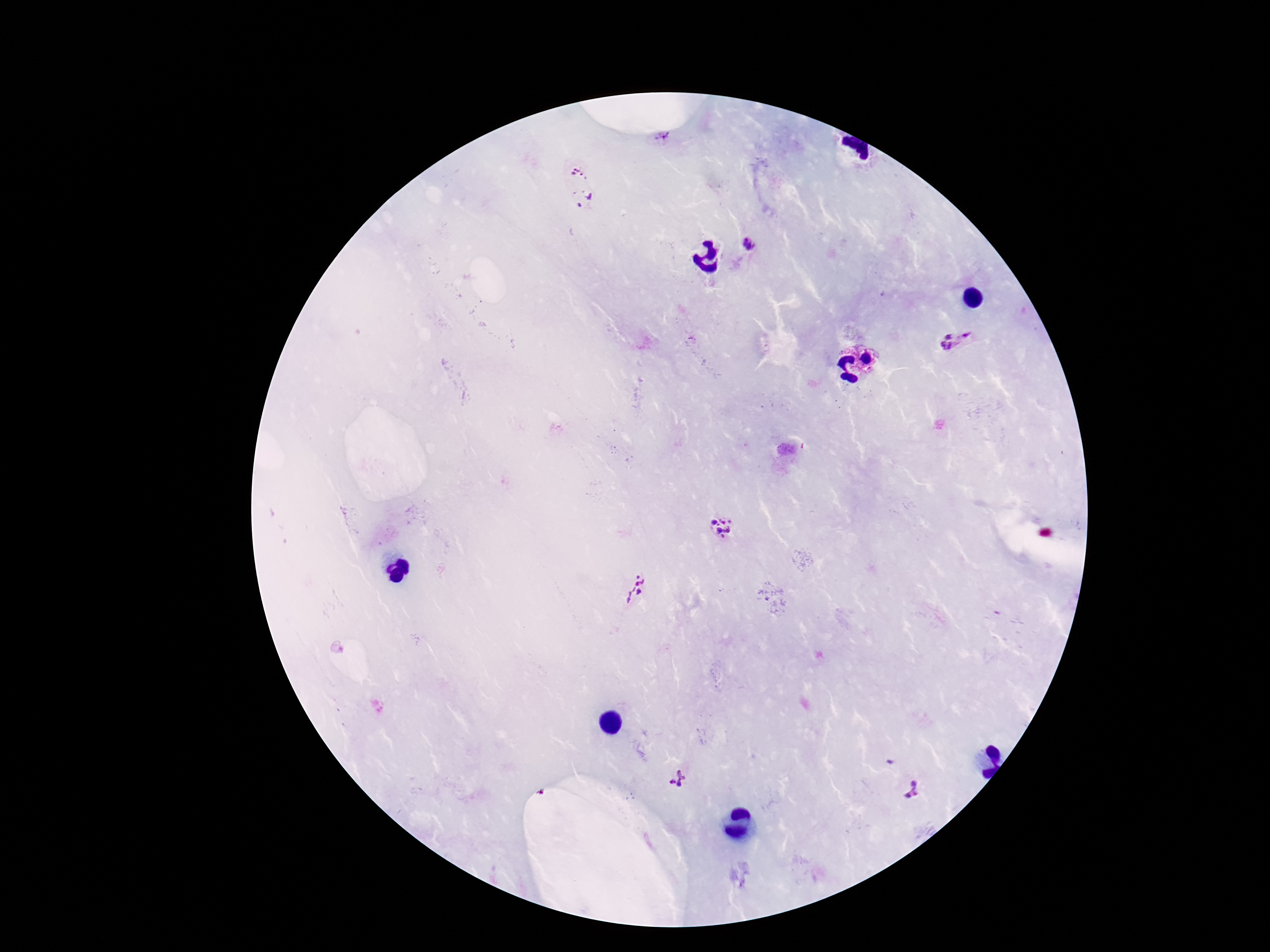
magnification = 100x
preparation = thick blood smear
stain = Giemsa
capture = smartphone camera through the microscope eyepiece
Plasmodium parasite locations = approximate centers as (x, y) in pixels: (664, 139), (579, 172), (590, 196), (578, 205), (747, 241), (967, 334), (945, 342), (722, 526), (635, 590), (678, 781), (912, 792)
image size = 1270×952 pixels
patient malaria status = positive
field of view = single